Classify this cell by malaria status.
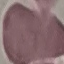
It is uninfected.

Summary:
  - Stain: Giemsa
  - Image type: cell patch, automatically extracted from a larger field of view and resized to 64 × 64 pixels
  - Capture: smartphone through the microscope eyepiece
  - Preparation: thin smear